Give the extent of all Plasmodium falciparum-infected red blood cells.
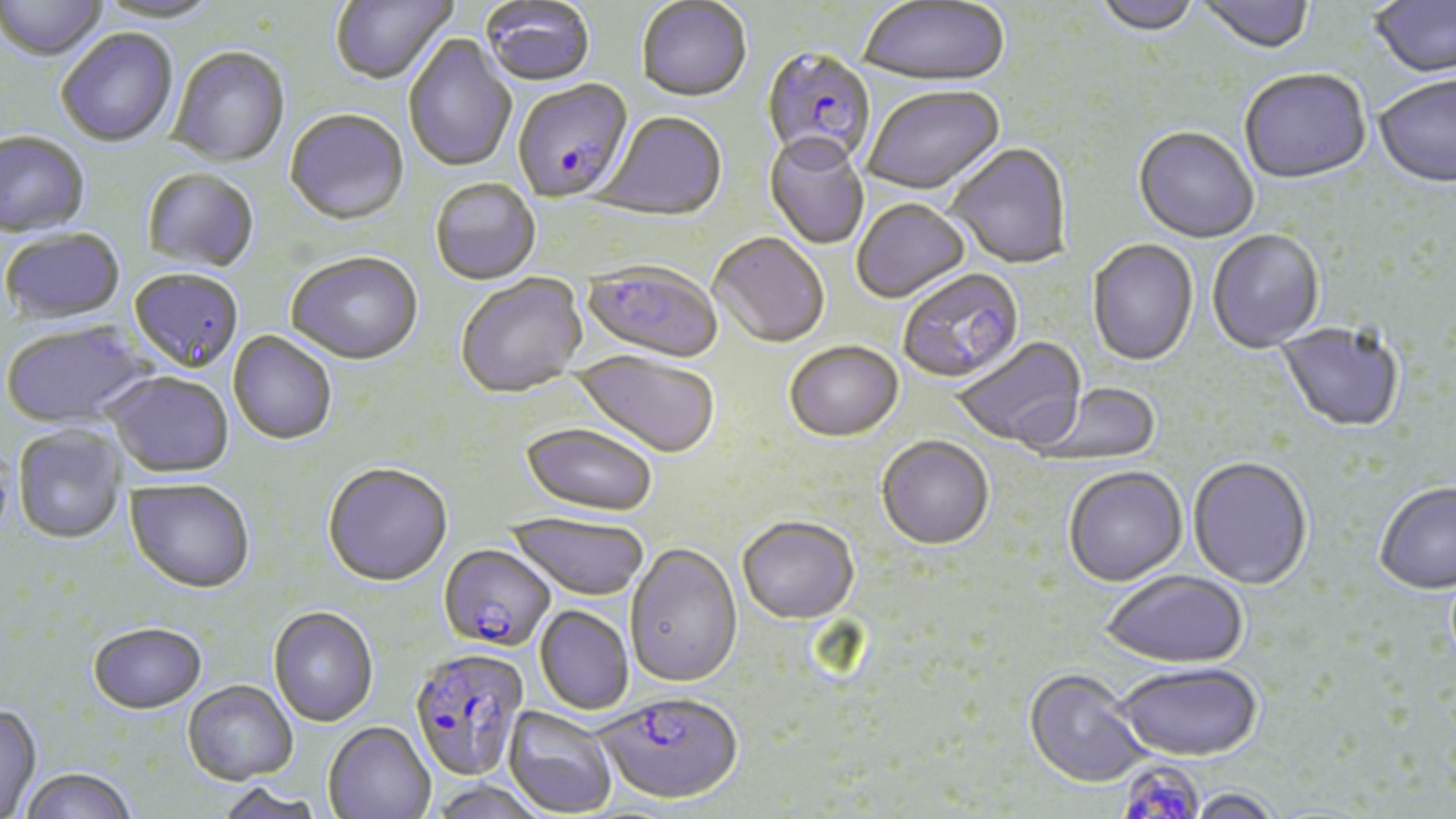

Approximate bounding boxes as (x1,y1)-(x2,y2) corner pairs in pixels.
Plasmodium falciparum-infected red blood cells: (761,47)-(877,171), (513,80)-(634,204), (582,259)-(723,363), (440,543)-(556,651), (408,646)-(530,781), (597,690)-(743,804), (1124,760)-(1207,819).

Uninfected red blood cell locations: (0,0)-(107,64), (93,0)-(225,26), (330,0)-(457,85), (1093,0)-(1200,39), (1196,0)-(1314,57), (1369,0)-(1456,80), (481,1)-(595,86), (636,1)-(752,102), (857,1)-(1009,89), (56,29)-(178,147), (404,34)-(517,173), (167,46)-(290,167), (1239,72)-(1372,187), (1374,77)-(1456,190), (863,87)-(1005,196), (284,108)-(409,224), (596,111)-(727,221), (1133,127)-(1259,244), (0,131)-(91,237), (764,133)-(870,249), (946,143)-(1072,269), (142,168)-(259,271), (430,179)-(541,285), (852,198)-(970,302), (2,227)-(126,324), (1207,230)-(1325,353), (709,232)-(830,347), (1087,239)-(1199,366), (286,250)-(423,363), (129,268)-(244,371), (897,268)-(1023,383), (456,274)-(587,397), (2,319)-(155,428), (1276,321)-(1405,432), (228,330)-(337,444), (952,336)-(1086,451), (784,340)-(903,441), (571,350)-(721,458), (105,371)-(234,477), (1031,381)-(1161,466), (521,421)-(659,516), (12,424)-(126,544), (876,435)-(994,548), (1188,456)-(1313,589), (322,461)-(453,585), (1062,465)-(1188,586), (126,478)-(255,592), (1373,480)-(1456,594), (505,513)-(650,601), (737,515)-(859,623), (625,541)-(742,687), (1100,569)-(1249,667), (535,605)-(634,714), (268,606)-(378,726), (88,621)-(206,713), (1113,662)-(1263,761), (1024,668)-(1153,788), (183,680)-(298,784), (0,703)-(42,817), (503,706)-(619,817), (323,720)-(436,819), (17,765)-(138,819), (430,779)-(551,819), (216,781)-(326,819), (1182,787)-(1286,819). Slide-level diagnosis: Plasmodium falciparum. One field of a larger specimen. May-Grünwald-Giemsa-stained preparation. Image is 1456×819 pixels. Captured at 1000x magnification. Light microscopy. Thin blood film.